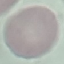

Result: negative for malaria parasites. Giemsa stain. Thin smear of blood. Photographed with a smartphone camera at the microscope eyepiece. Automatically extracted cell patch, resized to 64 × 64 pixels.